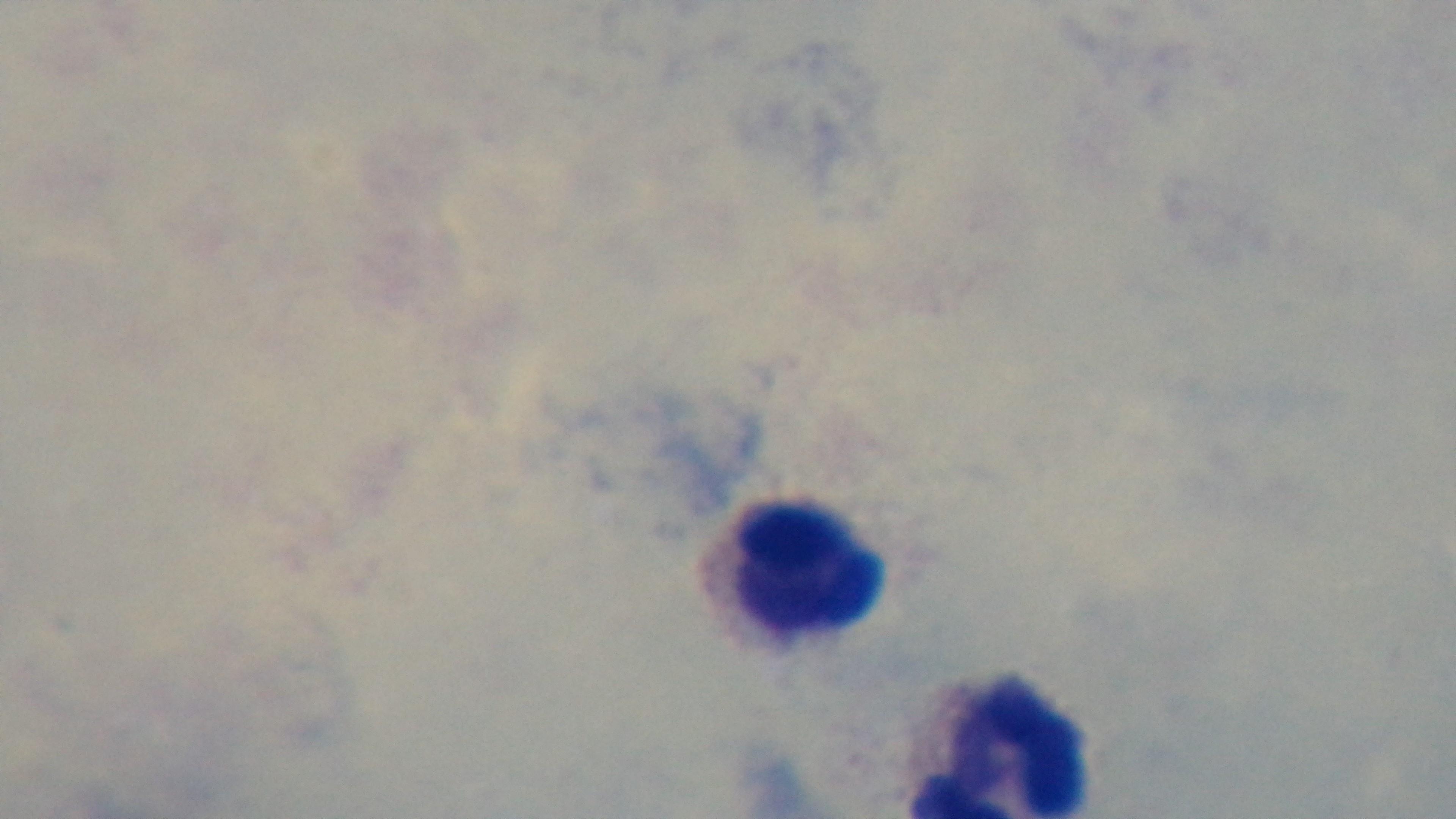
Summary:
  - Capture: mounted 4K digital camera
  - Field of view: one from the slide
  - Objective: 100x oil immersion
  - Preparation: thick
  - Stain: Giemsa
  - Malaria status: negative
  - Modality: light microscopy